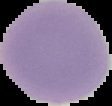

image_type: segmented cell region with the area outside set to black
preparation: thin blood film
image_size: 112×106 pixels
malaria_status: uninfected